State the blood parasite species.
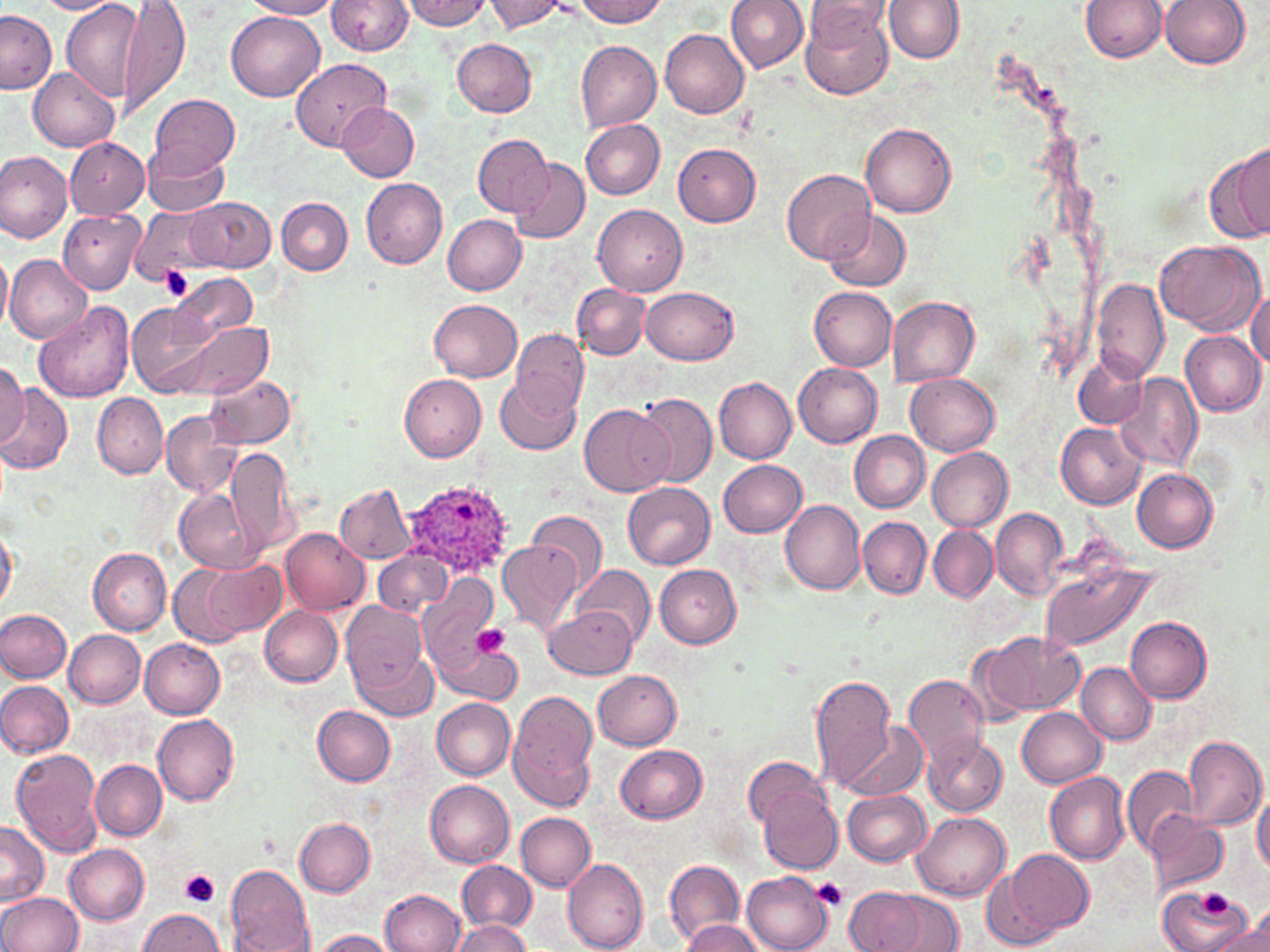

Plasmodium ovale.

uninfected red blood cell locations = approximate bounding boxes as [x1, y1, x2, y2] in pixels: [119, 0, 191, 118], [245, 0, 342, 19], [327, 0, 413, 56], [403, 0, 492, 29], [482, 0, 570, 35], [570, 0, 668, 27], [727, 0, 808, 71], [808, 0, 893, 48], [1081, 0, 1167, 62], [1160, 0, 1250, 69], [32, 1, 120, 14], [62, 1, 142, 100], [884, 1, 963, 62], [801, 6, 893, 101], [0, 10, 55, 96], [227, 12, 324, 101], [660, 29, 749, 118], [453, 39, 536, 117], [575, 40, 661, 131], [291, 57, 392, 150], [28, 66, 119, 151], [150, 94, 239, 176], [338, 101, 418, 180], [580, 119, 665, 198], [862, 124, 957, 218], [472, 134, 552, 216], [65, 138, 149, 219], [673, 144, 761, 226], [144, 145, 228, 215], [1217, 146, 1269, 241], [0, 151, 73, 243], [510, 159, 589, 245], [781, 170, 876, 266], [360, 178, 447, 269], [186, 196, 275, 271], [277, 198, 352, 274], [593, 202, 688, 296], [130, 205, 220, 284], [58, 207, 146, 294], [823, 210, 912, 293], [443, 214, 526, 295], [1156, 241, 1263, 334], [0, 252, 13, 334], [6, 254, 90, 343], [170, 271, 256, 342], [1092, 279, 1169, 382], [572, 285, 649, 359], [642, 286, 738, 364], [810, 287, 897, 370], [1247, 290, 1269, 370], [888, 296, 979, 386], [430, 299, 521, 383], [126, 300, 218, 398], [34, 301, 135, 404], [176, 320, 271, 401], [510, 327, 588, 418], [1181, 331, 1265, 416], [1073, 354, 1146, 429], [0, 359, 28, 448], [793, 362, 883, 447], [397, 370, 487, 461], [1114, 372, 1202, 475], [205, 373, 295, 449], [905, 374, 1000, 455], [496, 376, 582, 453], [714, 377, 797, 464], [0, 383, 72, 474], [94, 393, 168, 479], [633, 393, 718, 487], [580, 404, 673, 497], [161, 410, 239, 499], [1056, 422, 1146, 509], [850, 431, 929, 512], [225, 446, 299, 555], [928, 446, 1013, 531], [720, 459, 808, 537], [1133, 468, 1220, 552], [624, 482, 715, 570], [337, 484, 416, 562], [176, 489, 257, 572], [779, 499, 865, 594], [991, 507, 1067, 596], [527, 510, 608, 594], [858, 518, 931, 598], [0, 524, 18, 613], [929, 524, 997, 604], [280, 528, 370, 614], [498, 540, 581, 634], [374, 548, 451, 618], [89, 549, 171, 634], [202, 558, 285, 638], [1039, 562, 1161, 652], [169, 564, 246, 648], [656, 565, 741, 649], [576, 566, 655, 647], [420, 572, 501, 686], [340, 600, 430, 706], [546, 605, 637, 679], [260, 606, 342, 687], [0, 609, 71, 682], [1126, 617, 1212, 703], [64, 629, 146, 708], [975, 630, 1083, 718], [139, 638, 224, 718], [442, 646, 524, 704], [357, 653, 437, 719], [1077, 662, 1157, 744], [595, 670, 682, 750], [809, 673, 896, 794], [904, 673, 991, 772], [0, 681, 74, 758], [507, 690, 598, 811], [430, 698, 515, 780], [313, 705, 396, 785], [1017, 707, 1106, 788], [153, 712, 238, 805], [842, 719, 928, 802], [921, 732, 1007, 816], [1183, 734, 1267, 832], [616, 744, 708, 823], [11, 749, 103, 857], [744, 758, 835, 835], [92, 759, 167, 839], [1122, 764, 1196, 855], [1044, 771, 1130, 865], [425, 780, 514, 869], [755, 781, 843, 876], [1253, 788, 1270, 875], [844, 790, 931, 866], [1144, 810, 1227, 898], [913, 811, 1010, 899], [516, 813, 595, 891], [296, 818, 375, 896], [0, 821, 49, 906], [64, 844, 149, 926], [1008, 849, 1094, 935], [664, 859, 745, 950], [456, 860, 536, 933], [563, 860, 649, 951], [226, 864, 314, 951], [982, 865, 1066, 952], [742, 871, 833, 952], [1159, 886, 1255, 952], [841, 887, 938, 952], [380, 889, 466, 951], [879, 891, 964, 951], [0, 892, 82, 952], [1245, 906, 1268, 946], [138, 910, 226, 952], [451, 918, 529, 952], [679, 919, 766, 951], [1209, 923, 1269, 952], [307, 929, 401, 951]
Plasmodium ovale-infected red blood cell locations = approximate bounding boxes as [x1, y1, x2, y2] in pixels: [407, 481, 516, 577]
preparation = thin blood smear
field of view = one of a larger specimen
modality = light microscopy
image size = 1270×952 pixels
stain = May-Grünwald-Giemsa
platelet locations = approximate bounding boxes as [x1, y1, x2, y2] in pixels: [159, 266, 195, 302], [470, 623, 508, 659], [179, 870, 221, 909], [811, 877, 849, 911], [1201, 890, 1232, 919]
magnification = 1000x